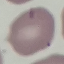
Summary:
  - Malaria status: uninfected
  - Capture: smartphone camera at the microscope eyepiece
  - Preparation: thin smear
  - Stain: Giemsa
  - Image type: automatically extracted cell patch, resized to 64 × 64 pixels